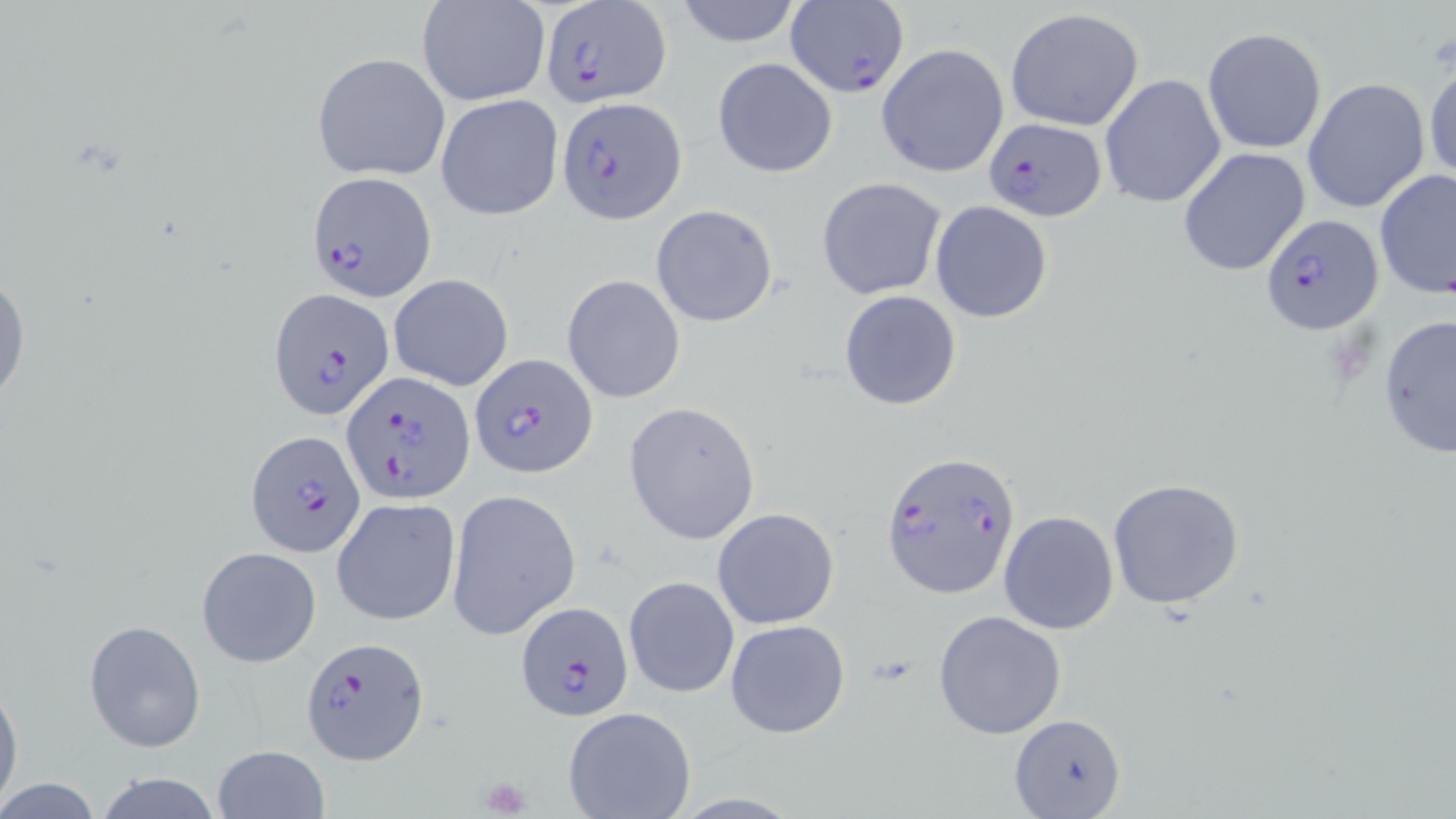

slide-level diagnosis = Plasmodium falciparum
uninfected red blood cell locations = approximate bounding boxes as named x1/y1/x2/y2 corners in pixels: (x1=671, y1=0, x2=807, y2=47), (x1=415, y1=1, x2=549, y2=108), (x1=1004, y1=8, x2=1146, y2=132), (x1=1203, y1=28, x2=1327, y2=154), (x1=877, y1=43, x2=1009, y2=178), (x1=312, y1=53, x2=450, y2=180), (x1=711, y1=56, x2=838, y2=178), (x1=1423, y1=56, x2=1456, y2=186), (x1=1099, y1=73, x2=1226, y2=211), (x1=1303, y1=78, x2=1431, y2=215), (x1=435, y1=93, x2=564, y2=221), (x1=1177, y1=148, x2=1312, y2=278), (x1=1374, y1=168, x2=1454, y2=302), (x1=815, y1=176, x2=947, y2=300), (x1=929, y1=201, x2=1054, y2=323), (x1=650, y1=204, x2=779, y2=327), (x1=0, y1=258, x2=29, y2=416), (x1=387, y1=273, x2=514, y2=391), (x1=562, y1=274, x2=686, y2=404), (x1=838, y1=291, x2=963, y2=411), (x1=1377, y1=314, x2=1456, y2=458), (x1=624, y1=401, x2=762, y2=545), (x1=1106, y1=478, x2=1246, y2=612), (x1=445, y1=488, x2=582, y2=641), (x1=332, y1=497, x2=460, y2=627), (x1=713, y1=508, x2=838, y2=629), (x1=998, y1=511, x2=1119, y2=634), (x1=196, y1=547, x2=321, y2=668), (x1=624, y1=576, x2=739, y2=699), (x1=933, y1=609, x2=1067, y2=740), (x1=83, y1=619, x2=206, y2=753), (x1=724, y1=619, x2=852, y2=740), (x1=0, y1=679, x2=22, y2=813), (x1=562, y1=707, x2=695, y2=819), (x1=1011, y1=711, x2=1124, y2=818), (x1=211, y1=745, x2=329, y2=819), (x1=89, y1=773, x2=229, y2=819), (x1=0, y1=778, x2=103, y2=816)
Plasmodium falciparum-infected red blood cell locations = approximate bounding boxes as named x1/y1/x2/y2 corners in pixels: (x1=536, y1=2, x2=674, y2=109), (x1=785, y1=5, x2=909, y2=99), (x1=559, y1=97, x2=687, y2=222), (x1=981, y1=118, x2=1108, y2=221), (x1=307, y1=170, x2=435, y2=299), (x1=1260, y1=214, x2=1382, y2=335), (x1=269, y1=288, x2=395, y2=420), (x1=469, y1=354, x2=595, y2=478), (x1=343, y1=371, x2=474, y2=502), (x1=246, y1=431, x2=365, y2=559), (x1=882, y1=454, x2=1019, y2=602), (x1=516, y1=599, x2=633, y2=721), (x1=301, y1=635, x2=433, y2=764)
preparation = thin blood film
stain = May-Grünwald-Giemsa
image size = 1456×819 pixels
platelet locations = approximate bounding boxes as named x1/y1/x2/y2 corners in pixels: (x1=477, y1=776, x2=533, y2=817)
field of view = single
magnification = 1000x
modality = light microscopy